Assess this cell for malaria.
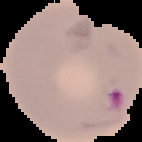
It is parasitized.

{
  "image_size": "142×142 pixels",
  "preparation": "thin blood film",
  "image_type": "cell region segmented out of the field of view; surrounding area masked to black"
}